Name the blood parasite species.
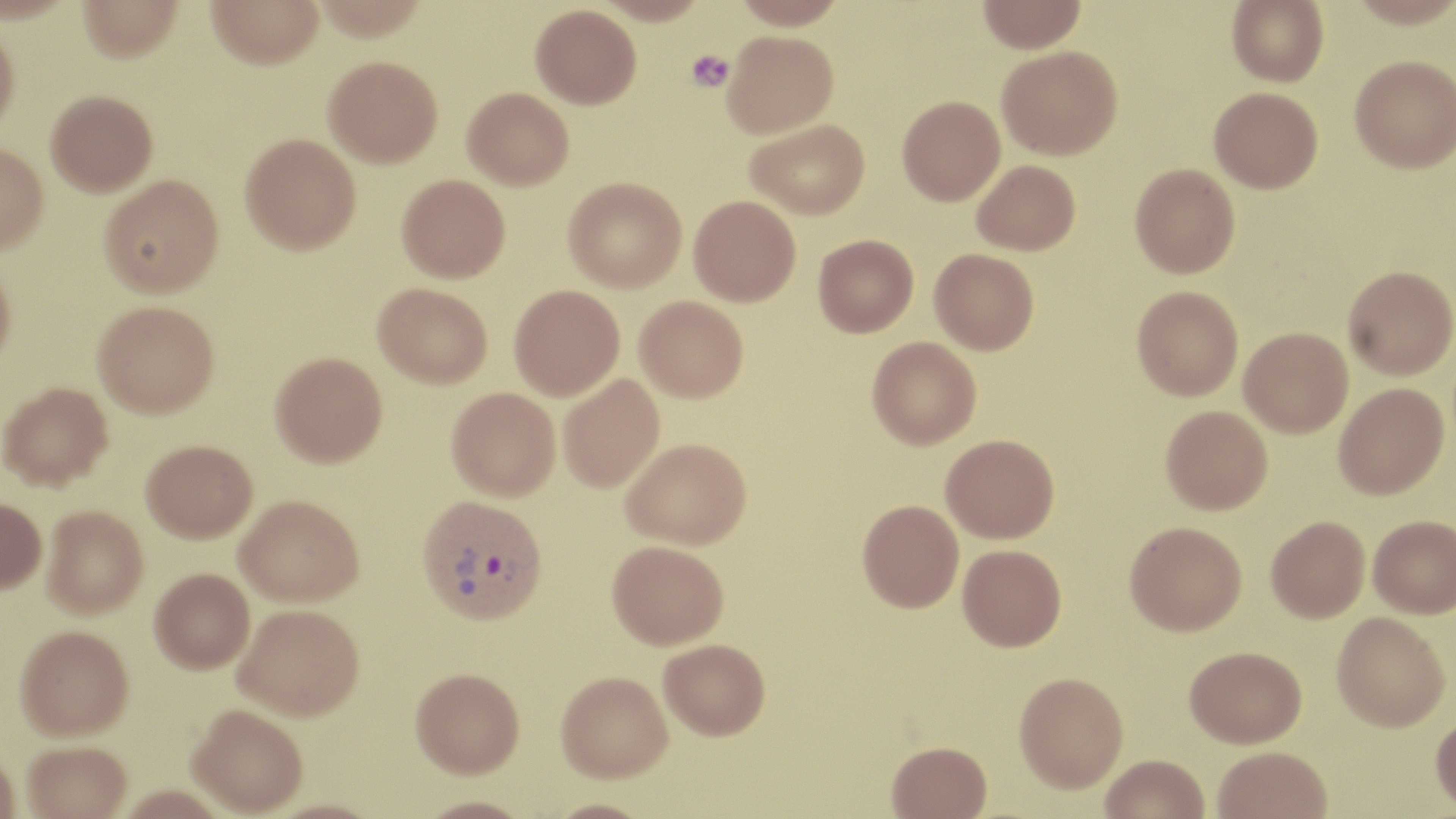
Plasmodium vivax.

Summary:
  - Coordinate format: approximate bounding boxes as [x1, y1, x2, y2] in pixels
  - Uninfected red blood cell locations: [77, 0, 184, 62], [207, 0, 323, 69], [732, 0, 846, 29], [977, 0, 1087, 53], [1226, 0, 1329, 87], [531, 4, 641, 108], [0, 21, 20, 140], [722, 30, 838, 138], [997, 45, 1123, 159], [1350, 54, 1456, 173], [323, 55, 443, 167], [462, 87, 574, 189], [1209, 87, 1323, 193], [46, 90, 158, 196], [897, 95, 1005, 205], [745, 119, 870, 219], [240, 132, 361, 253], [0, 142, 48, 255], [972, 159, 1080, 255], [1130, 163, 1240, 278], [99, 174, 223, 297], [397, 174, 510, 282], [563, 177, 686, 292], [689, 195, 801, 306], [813, 234, 919, 337], [929, 248, 1039, 355], [0, 261, 16, 374], [1343, 265, 1456, 379], [373, 282, 492, 388], [509, 284, 624, 400], [1132, 286, 1243, 400], [635, 295, 748, 402], [93, 300, 218, 417], [1239, 327, 1353, 437], [867, 336, 981, 449], [270, 351, 387, 467], [558, 374, 665, 493], [0, 381, 113, 490], [1334, 383, 1448, 499], [446, 387, 560, 501], [1161, 405, 1273, 515], [940, 434, 1059, 543], [622, 437, 751, 550], [141, 439, 257, 542], [235, 495, 362, 608], [0, 498, 46, 594], [858, 499, 964, 612], [41, 506, 148, 619], [1368, 515, 1456, 618], [1266, 516, 1370, 622], [1125, 521, 1247, 634], [607, 541, 728, 651], [958, 544, 1067, 651], [150, 568, 255, 674], [233, 606, 364, 724], [1331, 612, 1450, 732], [15, 627, 133, 743], [658, 639, 770, 743], [1185, 645, 1306, 747], [410, 670, 524, 782], [1014, 672, 1128, 795], [555, 675, 672, 787], [188, 707, 307, 818], [1430, 712, 1456, 815], [886, 743, 992, 819], [22, 744, 132, 819], [1213, 746, 1332, 819], [0, 750, 21, 819], [1101, 755, 1210, 819], [415, 798, 536, 819], [542, 800, 657, 819]
  - Platelet locations: [686, 49, 735, 92]
  - Plasmodium vivax-infected red blood cell locations: [417, 494, 548, 627]
  - Field of view: one of a larger specimen
  - Modality: light microscopy
  - Preparation: thin blood film
  - Stain: May-Grünwald-Giemsa
  - Image size: 1456×819 pixels
  - Magnification: 1000x